Name the cell type shown.
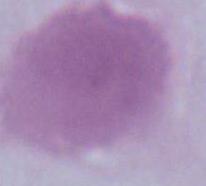

An erythrocyte.

magnification = 1000x
modality = photomicrograph